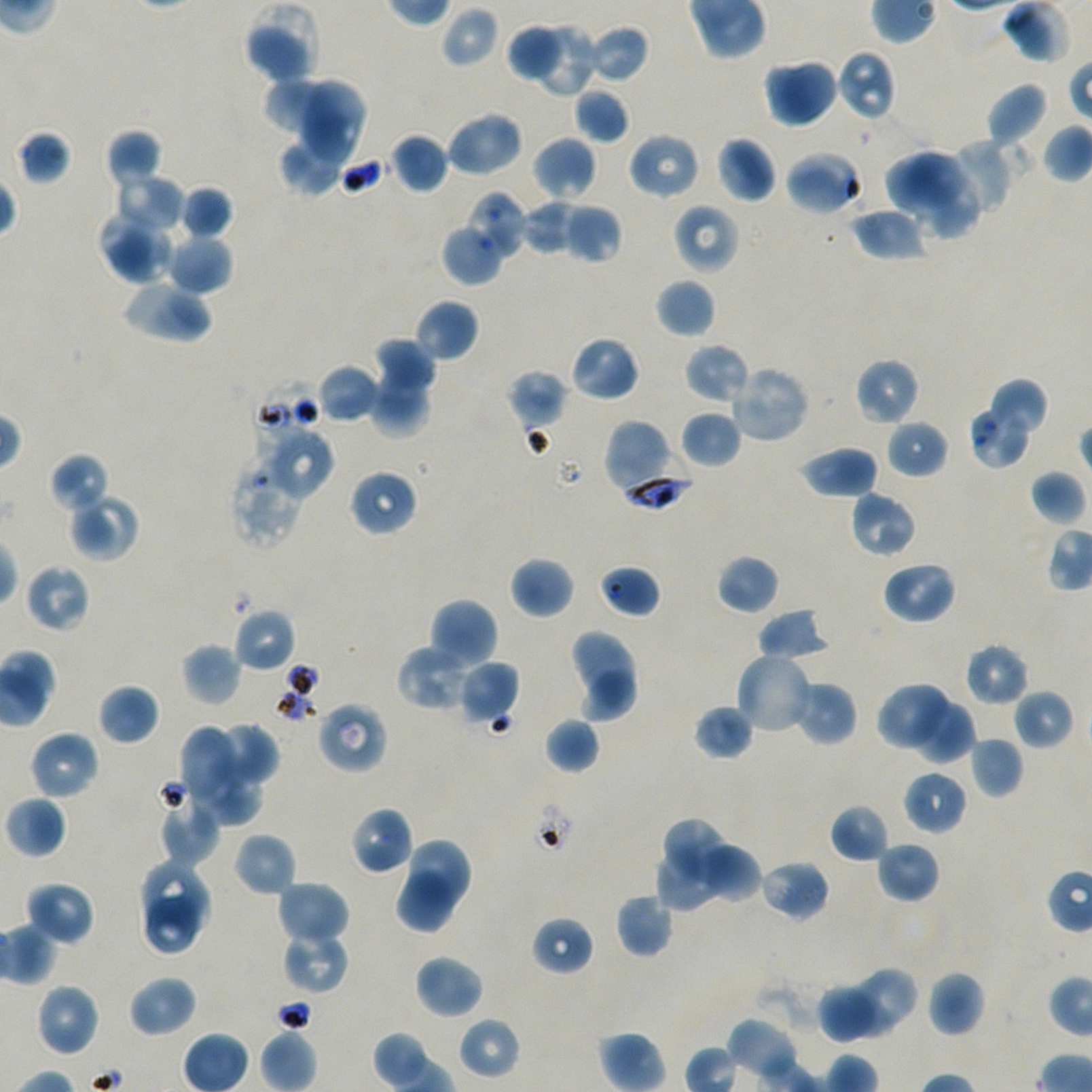

Approximate bounding boxes as (x1, y1, x2, y2) in pixels. Not every red blood cell is marked.
Summary:
  - Locations of uninfected red blood cells: (1001, 0, 1075, 64), (245, 5, 321, 84), (439, 5, 500, 69), (507, 20, 565, 83), (532, 22, 598, 99), (585, 24, 650, 84), (836, 50, 896, 122), (764, 57, 839, 128), (266, 76, 350, 145), (300, 79, 366, 164), (985, 82, 1049, 149), (575, 87, 631, 144), (444, 111, 524, 178), (16, 130, 72, 185), (104, 130, 162, 187), (627, 132, 701, 200), (391, 133, 449, 194), (278, 134, 348, 197), (714, 135, 777, 204), (531, 136, 597, 201), (945, 137, 1019, 215), (784, 149, 864, 216), (885, 149, 970, 219), (908, 168, 981, 240), (113, 172, 185, 232), (179, 185, 233, 239), (466, 190, 530, 261), (521, 199, 578, 255), (672, 203, 740, 275), (563, 204, 622, 264), (850, 206, 926, 261), (98, 209, 175, 284), (441, 224, 504, 286), (166, 232, 234, 295), (121, 277, 213, 343), (655, 278, 716, 338), (414, 298, 480, 363), (570, 335, 640, 402), (374, 338, 436, 393), (684, 342, 750, 404), (854, 357, 920, 426), (317, 364, 381, 423), (369, 365, 431, 441), (728, 365, 810, 443), (507, 369, 568, 427), (979, 378, 1050, 454), (968, 403, 1032, 469), (680, 410, 743, 468), (602, 418, 676, 492), (885, 420, 947, 478), (799, 444, 880, 500), (49, 452, 111, 514), (349, 469, 418, 536), (1029, 469, 1087, 527), (849, 490, 917, 558), (67, 492, 139, 561), (716, 554, 780, 615), (509, 556, 575, 619), (881, 560, 956, 625), (24, 564, 92, 633), (599, 564, 661, 619), (427, 598, 498, 670), (232, 606, 296, 673), (756, 606, 832, 662), (568, 628, 638, 708), (964, 642, 1030, 706), (182, 643, 242, 706), (397, 646, 478, 710), (734, 651, 814, 735), (457, 659, 520, 726), (575, 668, 637, 723), (791, 679, 858, 747), (876, 682, 953, 752), (98, 683, 159, 746), (1013, 688, 1075, 749), (908, 696, 975, 764), (315, 700, 388, 774), (693, 704, 754, 761), (544, 718, 600, 774), (208, 721, 278, 788), (179, 726, 250, 815), (29, 730, 99, 800), (970, 737, 1023, 798), (902, 769, 968, 835), (156, 787, 221, 866), (4, 795, 67, 858), (829, 804, 891, 862), (350, 806, 414, 875), (665, 818, 736, 886), (233, 832, 297, 897), (408, 837, 473, 908), (875, 841, 941, 903), (695, 842, 762, 903), (656, 844, 718, 912), (141, 856, 213, 932), (758, 858, 830, 922), (393, 869, 455, 934), (276, 880, 350, 947), (24, 881, 94, 945), (615, 893, 674, 958), (143, 896, 205, 956), (531, 916, 595, 975), (282, 930, 350, 994), (414, 953, 485, 1019), (860, 966, 917, 1024), (927, 970, 985, 1037), (128, 975, 198, 1038), (841, 976, 898, 1039), (34, 982, 101, 1057), (818, 984, 877, 1046), (458, 1017, 521, 1079), (726, 1017, 799, 1081)
  - Locations of infected red blood cells: (620, 445, 692, 513)
  - Locations of red blood cells of indeterminate infection status: (253, 379, 321, 447), (260, 427, 334, 500), (231, 458, 307, 547)
  - Preparation: thin blood film
  - Image size: 1092×1092 pixels
  - Culture: Plasmodium falciparum strain NF54, static, in vitro
  - Objective: 100x, oil immersion, numerical aperture 1.45
  - Stain: Giemsa
  - Field of view: one from this slide
  - Donor blood group: A+/O+